Report the malaria status of this cell.
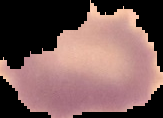
It is uninfected.

Summary:
  - Image type: segmented cell region with the area outside set to black
  - Image size: 163×118 pixels
  - Preparation: thin blood film